Report the malaria status of this cell.
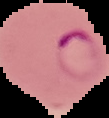

It is parasitized.

From a thin blood smear. Image is 109×118 pixels. The area outside the segmented cell region is set to black.